Classify this cell by malaria status.
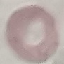
Uninfected.

preparation = thin blood film
capture = smartphone camera at the microscope eyepiece
image type = automatically extracted cell patch, resized to 64 × 64 pixels
stain = Giemsa